Identify the blood parasite species.
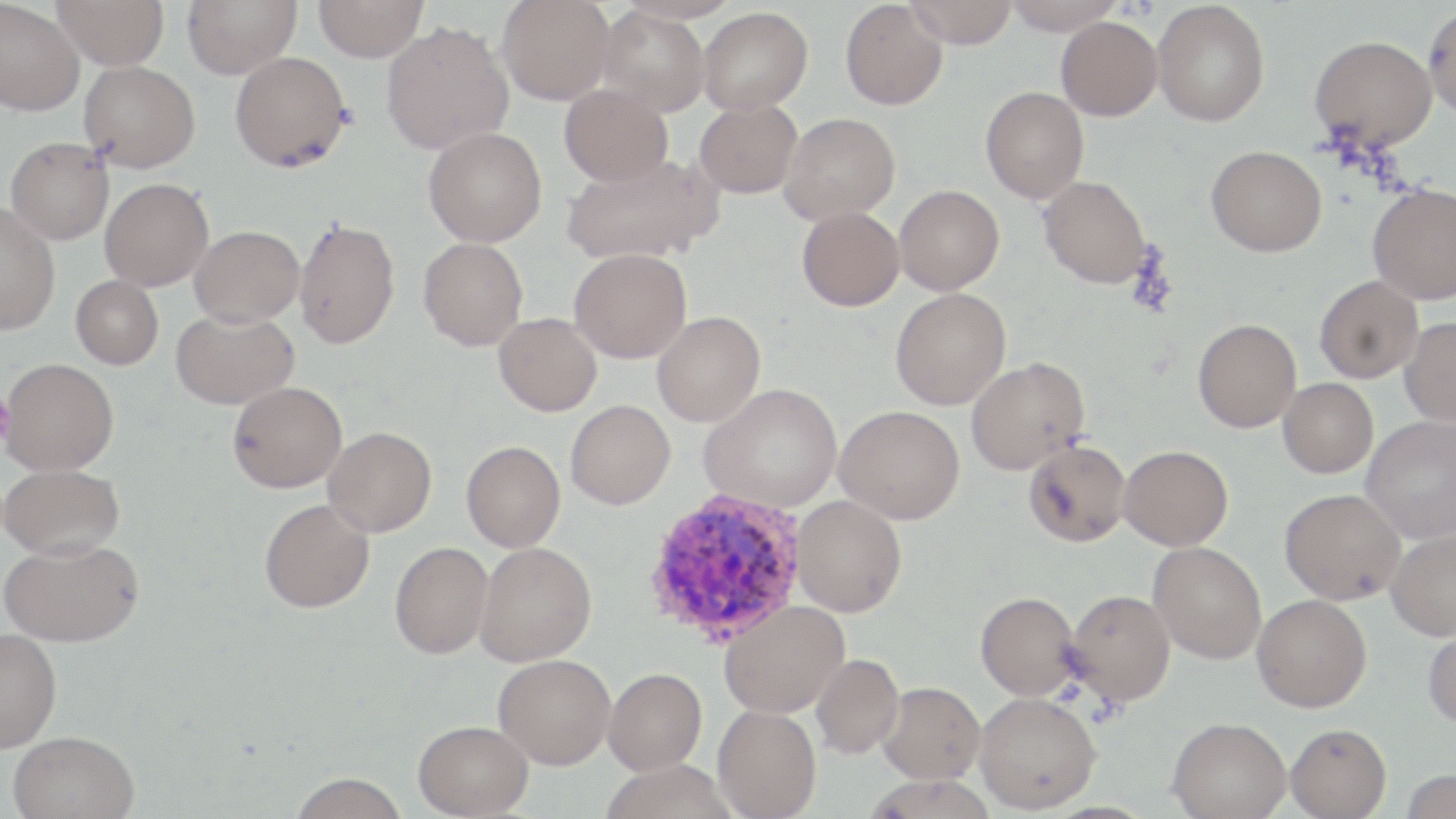

Plasmodium vivax.

Approximate bounding boxes as (x1, y1, x2, y2) in pixels. Platelet locations: (0, 397, 14, 442). Plasmodium vivax-infected red blood cell locations: (644, 488, 808, 645). Uninfected red blood cell locations: (52, 0, 169, 70), (182, 0, 300, 78), (314, 0, 428, 62), (497, 0, 614, 105), (904, 0, 1019, 47), (1000, 0, 1125, 34), (840, 1, 947, 111), (1152, 1, 1270, 127), (0, 2, 85, 116), (1423, 4, 1456, 120), (596, 7, 710, 116), (698, 7, 813, 114), (1056, 17, 1162, 120), (381, 20, 514, 154), (1309, 35, 1437, 152), (229, 51, 351, 172), (79, 60, 200, 172), (559, 84, 673, 187), (980, 87, 1088, 203), (694, 100, 802, 199), (779, 112, 900, 224), (423, 126, 547, 247), (5, 137, 114, 245), (1205, 145, 1326, 257), (561, 152, 722, 266), (1038, 176, 1152, 289), (100, 178, 213, 291), (1367, 183, 1456, 305), (894, 185, 1005, 295), (0, 204, 60, 334), (796, 206, 904, 311), (294, 217, 400, 349), (189, 225, 303, 327), (418, 237, 528, 351), (569, 248, 691, 363), (1314, 275, 1423, 383), (71, 276, 163, 369), (890, 288, 1010, 410), (171, 309, 298, 410), (652, 311, 765, 427), (493, 313, 602, 416), (1399, 316, 1456, 427), (1193, 318, 1301, 433), (965, 357, 1090, 474), (1, 358, 119, 475), (1278, 378, 1378, 478), (228, 381, 347, 493), (700, 383, 842, 513), (565, 400, 675, 509), (834, 405, 964, 524), (1361, 415, 1456, 543), (323, 426, 436, 537), (1023, 439, 1130, 547), (461, 441, 565, 552), (1118, 445, 1233, 550), (0, 463, 125, 560), (1279, 488, 1405, 604), (791, 495, 907, 617), (260, 499, 374, 612), (1385, 527, 1456, 640), (1, 537, 145, 647), (1148, 541, 1266, 664), (389, 542, 493, 659), (473, 542, 596, 666), (1065, 588, 1176, 705), (975, 591, 1080, 700), (1252, 594, 1371, 712), (719, 599, 849, 718), (1423, 623, 1456, 731), (0, 628, 62, 752), (811, 653, 904, 759), (493, 654, 615, 769), (604, 668, 707, 775), (878, 681, 985, 784), (974, 692, 1101, 813), (712, 705, 821, 819), (1168, 716, 1292, 818), (413, 719, 533, 818), (1285, 722, 1392, 819), (8, 730, 139, 819), (601, 760, 734, 819), (289, 773, 409, 818). 1000x magnification. May-Grünwald-Giemsa stain. Optical microscopy. Thin blood film. One field of a larger specimen. Image is 1456×819 pixels.